Identify the blood parasite species.
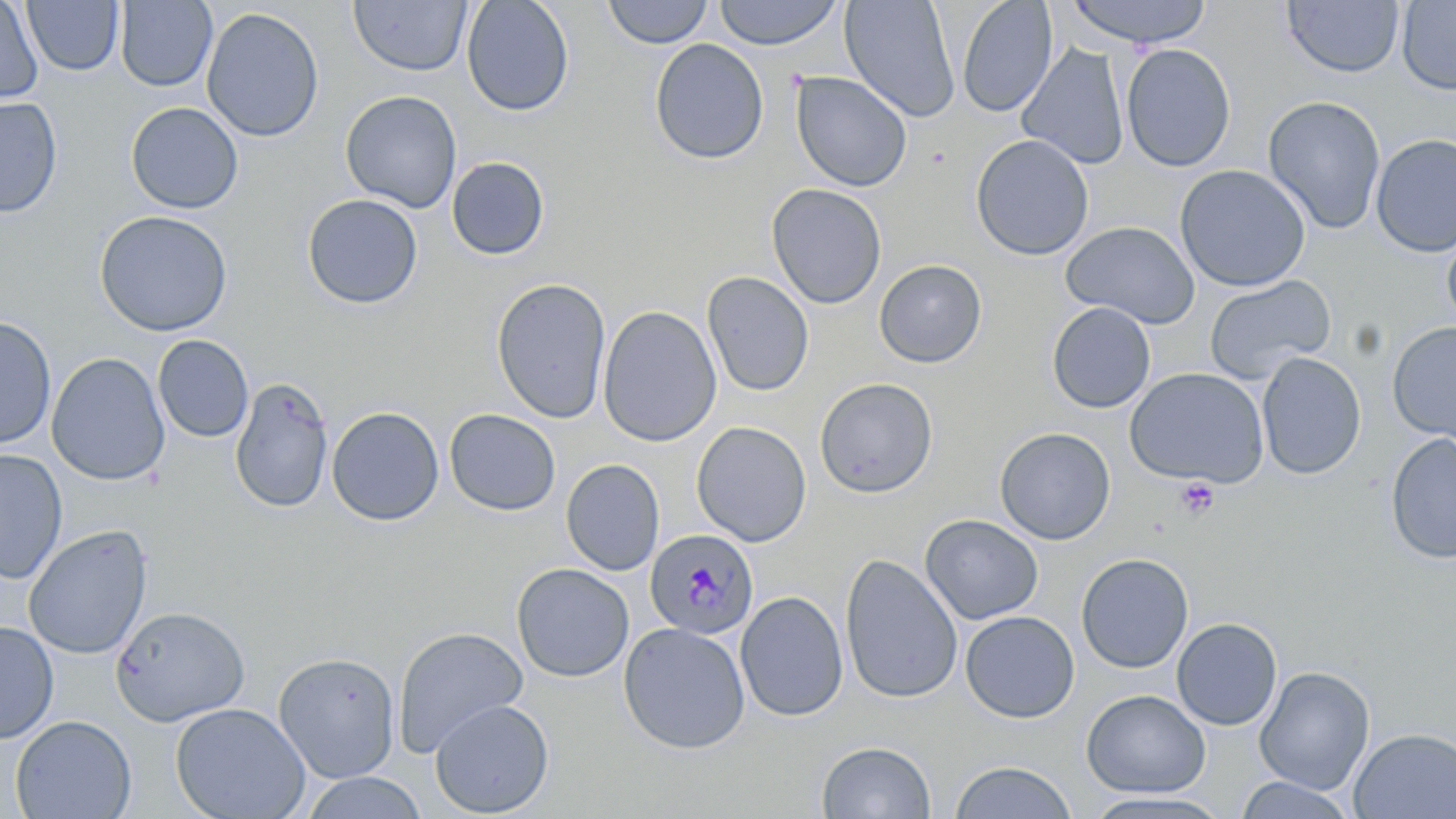
Plasmodium malariae.

Approximate bounding boxes as (x1, y1, x2, y2) in pixels. Platelet locations: (1153, 468, 1238, 523), (1175, 478, 1219, 520). Plasmodium malariae-infected red blood cell locations: (647, 529, 760, 642). Uninfected red blood cell locations: (115, 0, 218, 92), (348, 0, 473, 77), (460, 0, 575, 117), (712, 0, 844, 50), (840, 0, 961, 122), (956, 0, 1058, 117), (1064, 0, 1213, 48), (1397, 0, 1456, 95), (0, 1, 43, 105), (22, 1, 125, 76), (601, 1, 714, 49), (1282, 1, 1404, 79), (201, 7, 325, 143), (649, 38, 769, 165), (1018, 43, 1130, 171), (1120, 43, 1236, 172), (790, 71, 912, 192), (340, 90, 463, 213), (1262, 95, 1386, 235), (0, 97, 63, 217), (125, 101, 244, 214), (971, 133, 1094, 260), (1370, 133, 1456, 257), (446, 156, 550, 261), (1174, 164, 1311, 291), (766, 183, 887, 309), (301, 193, 423, 309), (94, 209, 233, 337), (1061, 221, 1200, 328), (1441, 222, 1456, 334), (873, 259, 988, 368), (702, 271, 815, 396), (1203, 275, 1336, 384), (490, 277, 611, 424), (1046, 302, 1156, 413), (597, 305, 722, 447), (0, 316, 58, 450), (1387, 321, 1456, 445), (152, 335, 254, 443), (46, 352, 170, 486), (1256, 352, 1366, 480), (1124, 367, 1270, 487), (230, 376, 334, 513), (814, 377, 938, 498), (326, 406, 444, 526), (444, 409, 561, 516), (691, 421, 812, 546), (994, 426, 1116, 545), (1385, 433, 1456, 564), (0, 448, 68, 585), (561, 459, 665, 576), (920, 514, 1043, 625), (23, 524, 153, 660), (1076, 552, 1194, 673), (840, 553, 963, 704), (511, 563, 634, 682), (735, 590, 848, 722), (110, 606, 250, 727), (960, 610, 1080, 723), (1171, 617, 1283, 731), (0, 621, 59, 744), (618, 621, 750, 754), (392, 625, 529, 757), (273, 652, 400, 783), (1253, 666, 1375, 795), (1081, 689, 1211, 797), (429, 698, 554, 817), (170, 702, 310, 819), (10, 715, 136, 819), (1348, 727, 1456, 819), (817, 740, 937, 818), (949, 760, 1077, 818), (299, 772, 428, 819), (1235, 776, 1358, 818), (1081, 791, 1233, 818). Thin blood film. May-Grünwald-Giemsa-stained preparation. Optical microscopy. 1000x magnification. Image is 1456×819 pixels. Single field of view.